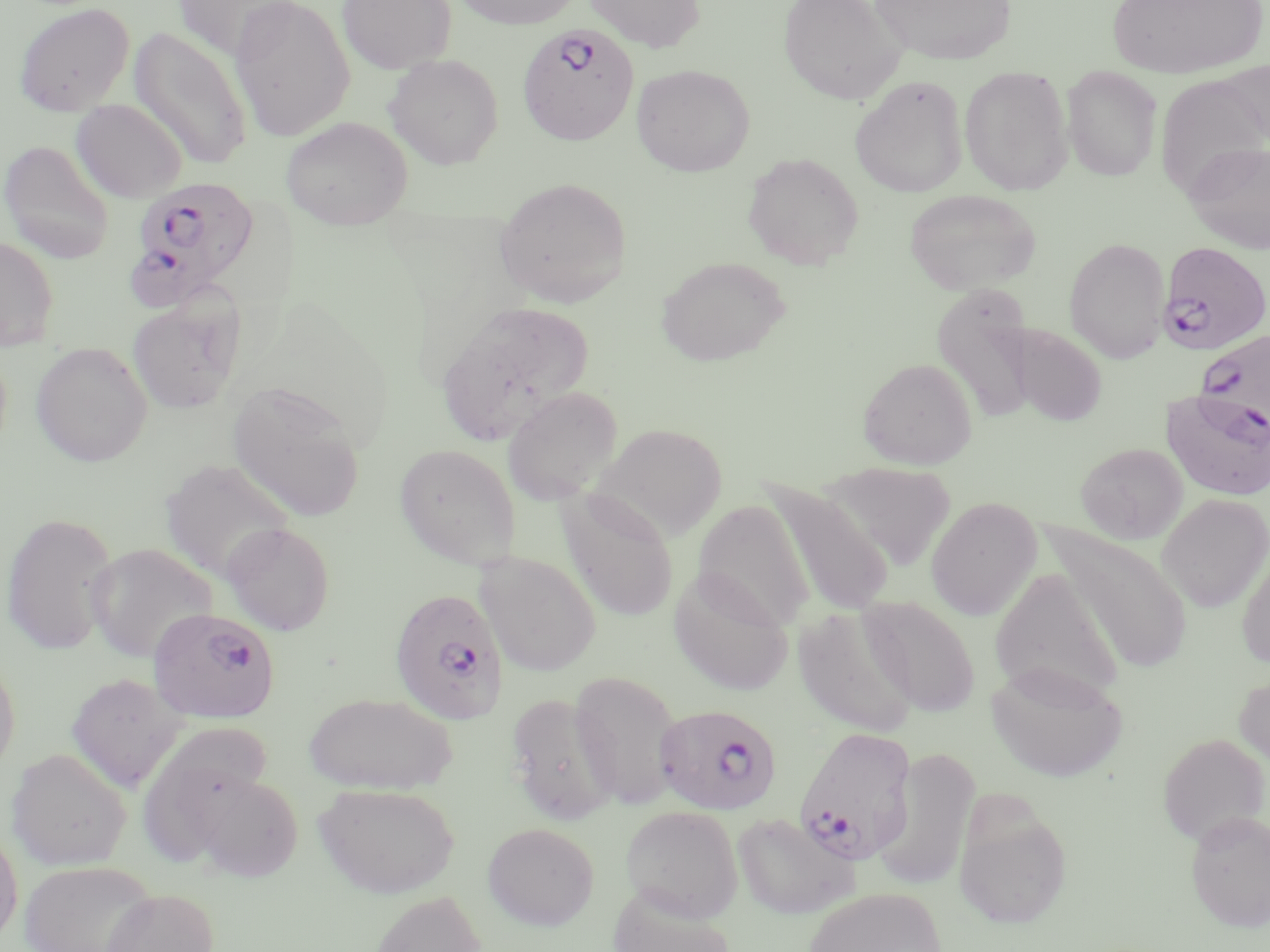

slide-level diagnosis = Plasmodium falciparum
field of view = single
uninfected red blood cell locations = approximate bounding boxes as named x1/y1/x2/y2 corners in pixels: (x1=229, y1=0, x2=355, y2=141), (x1=336, y1=0, x2=457, y2=73), (x1=450, y1=0, x2=583, y2=29), (x1=583, y1=0, x2=706, y2=52), (x1=777, y1=0, x2=906, y2=106), (x1=870, y1=0, x2=1017, y2=66), (x1=172, y1=1, x2=303, y2=61), (x1=1106, y1=1, x2=1268, y2=78), (x1=13, y1=2, x2=135, y2=117), (x1=130, y1=27, x2=253, y2=170), (x1=384, y1=54, x2=503, y2=170), (x1=631, y1=64, x2=754, y2=177), (x1=959, y1=66, x2=1073, y2=195), (x1=1061, y1=66, x2=1162, y2=181), (x1=1159, y1=74, x2=1269, y2=189), (x1=850, y1=75, x2=968, y2=198), (x1=71, y1=99, x2=188, y2=203), (x1=281, y1=116, x2=412, y2=231), (x1=0, y1=140, x2=115, y2=264), (x1=1183, y1=140, x2=1270, y2=254), (x1=742, y1=152, x2=864, y2=270), (x1=494, y1=176, x2=632, y2=307), (x1=904, y1=188, x2=1041, y2=294), (x1=0, y1=236, x2=60, y2=350), (x1=1063, y1=237, x2=1170, y2=363), (x1=656, y1=256, x2=791, y2=366), (x1=931, y1=284, x2=1038, y2=426), (x1=127, y1=293, x2=245, y2=414), (x1=436, y1=300, x2=595, y2=444), (x1=1011, y1=325, x2=1107, y2=426), (x1=31, y1=341, x2=153, y2=467), (x1=858, y1=357, x2=978, y2=469), (x1=228, y1=381, x2=366, y2=523), (x1=502, y1=387, x2=623, y2=505), (x1=1161, y1=387, x2=1270, y2=501), (x1=592, y1=422, x2=728, y2=540), (x1=1076, y1=442, x2=1188, y2=544), (x1=394, y1=443, x2=521, y2=568), (x1=159, y1=458, x2=294, y2=583), (x1=822, y1=461, x2=956, y2=573), (x1=764, y1=482, x2=894, y2=617), (x1=557, y1=490, x2=679, y2=622), (x1=1157, y1=493, x2=1270, y2=613), (x1=925, y1=497, x2=1042, y2=621), (x1=693, y1=500, x2=815, y2=631), (x1=1, y1=511, x2=119, y2=655), (x1=221, y1=522, x2=335, y2=636), (x1=1044, y1=524, x2=1194, y2=674), (x1=1235, y1=538, x2=1270, y2=668), (x1=86, y1=543, x2=217, y2=664), (x1=476, y1=552, x2=601, y2=677), (x1=669, y1=568, x2=795, y2=696), (x1=990, y1=568, x2=1123, y2=705), (x1=860, y1=596, x2=980, y2=716), (x1=793, y1=604, x2=917, y2=738), (x1=0, y1=656, x2=20, y2=777), (x1=986, y1=662, x2=1127, y2=782), (x1=1233, y1=669, x2=1270, y2=779), (x1=569, y1=670, x2=684, y2=809), (x1=66, y1=672, x2=187, y2=792), (x1=303, y1=692, x2=457, y2=794), (x1=505, y1=692, x2=619, y2=825), (x1=145, y1=720, x2=275, y2=858), (x1=1157, y1=732, x2=1269, y2=847), (x1=6, y1=747, x2=131, y2=870), (x1=872, y1=747, x2=980, y2=892), (x1=192, y1=771, x2=304, y2=882), (x1=314, y1=782, x2=460, y2=898), (x1=952, y1=801, x2=1073, y2=930), (x1=620, y1=805, x2=743, y2=921), (x1=1184, y1=811, x2=1270, y2=932), (x1=732, y1=812, x2=859, y2=921), (x1=0, y1=822, x2=23, y2=947), (x1=482, y1=822, x2=599, y2=930), (x1=20, y1=861, x2=156, y2=952), (x1=606, y1=886, x2=739, y2=952), (x1=802, y1=886, x2=949, y2=952), (x1=100, y1=887, x2=219, y2=952), (x1=368, y1=889, x2=487, y2=951)
Plasmodium falciparum-infected red blood cell locations = approximate bounding boxes as named x1/y1/x2/y2 corners in pixels: (x1=515, y1=24, x2=638, y2=148), (x1=125, y1=182, x2=255, y2=306), (x1=1158, y1=241, x2=1270, y2=354), (x1=1194, y1=326, x2=1270, y2=440), (x1=388, y1=588, x2=509, y2=725), (x1=147, y1=607, x2=280, y2=724), (x1=655, y1=704, x2=783, y2=816), (x1=793, y1=725, x2=917, y2=867)
stain = May-Grünwald-Giemsa
magnification = 1000x
modality = optical microscopy
preparation = thin blood film
image size = 1270×952 pixels